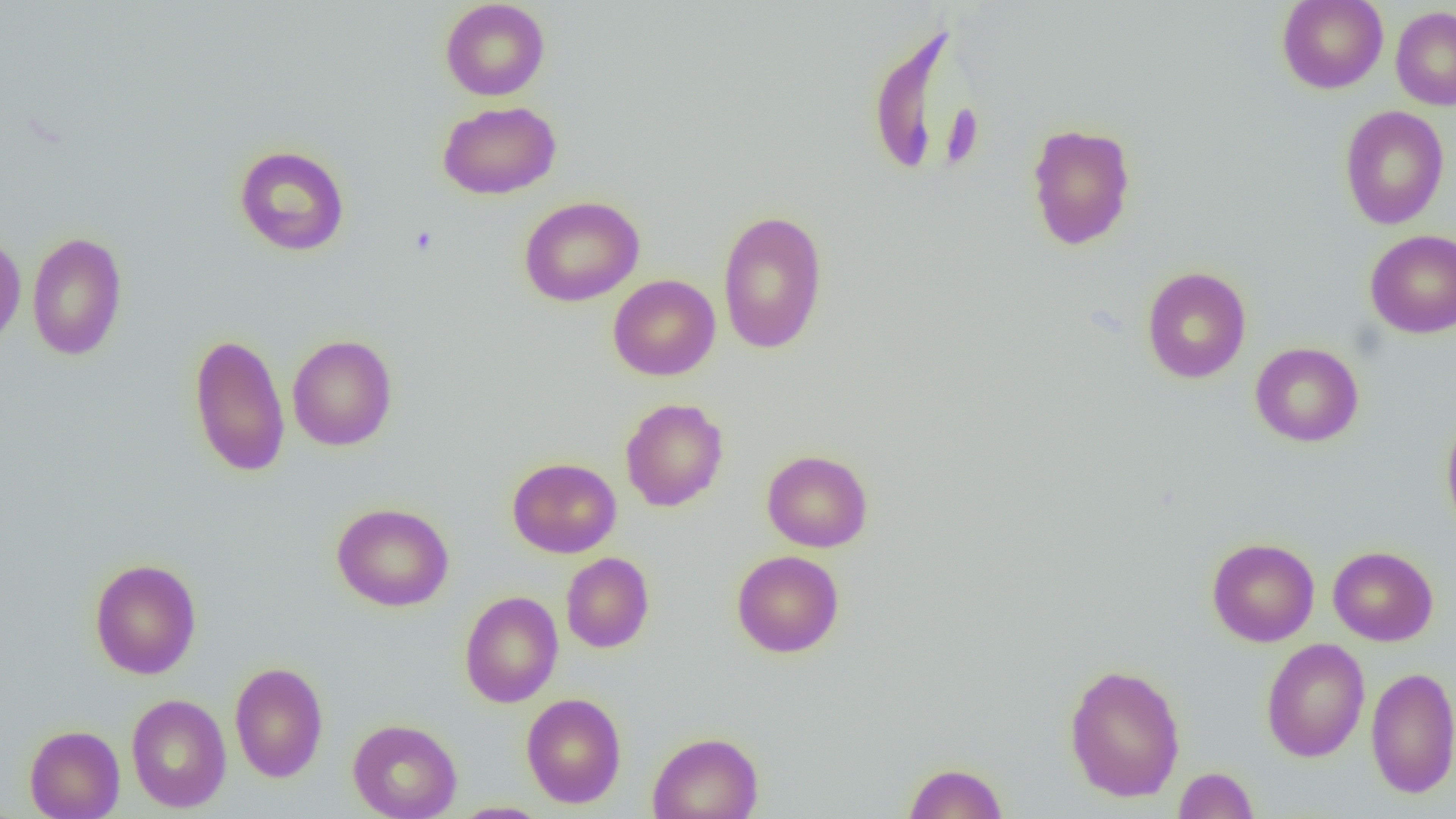

{
  "slide_level_diagnosis": "negative for blood parasites",
  "preparation": "thin blood film",
  "magnification": "1000x",
  "modality": "light microscopy",
  "uninfected_red_blood_cell_locations": "approximate bounding boxes as named x1/y1/x2/y2 corners in pixels: (x1=440, y1=0, x2=550, y2=101), (x1=1277, y1=0, x2=1388, y2=93), (x1=1390, y1=6, x2=1456, y2=110), (x1=867, y1=25, x2=971, y2=180), (x1=437, y1=101, x2=562, y2=199), (x1=1339, y1=105, x2=1450, y2=229), (x1=1026, y1=122, x2=1137, y2=251), (x1=234, y1=145, x2=350, y2=256), (x1=519, y1=195, x2=644, y2=306), (x1=717, y1=209, x2=828, y2=355), (x1=1364, y1=229, x2=1456, y2=337), (x1=27, y1=231, x2=128, y2=361), (x1=0, y1=232, x2=26, y2=350), (x1=1142, y1=266, x2=1251, y2=384), (x1=608, y1=274, x2=720, y2=380), (x1=188, y1=332, x2=291, y2=478), (x1=287, y1=334, x2=398, y2=451), (x1=1250, y1=342, x2=1363, y2=447), (x1=620, y1=398, x2=729, y2=512), (x1=1441, y1=414, x2=1456, y2=539), (x1=762, y1=450, x2=873, y2=553), (x1=507, y1=457, x2=621, y2=558), (x1=331, y1=502, x2=454, y2=612), (x1=1207, y1=537, x2=1319, y2=647), (x1=1327, y1=546, x2=1438, y2=646), (x1=731, y1=550, x2=844, y2=658), (x1=561, y1=552, x2=654, y2=653), (x1=89, y1=558, x2=202, y2=679), (x1=459, y1=590, x2=563, y2=708), (x1=1261, y1=638, x2=1370, y2=762), (x1=229, y1=661, x2=328, y2=783), (x1=1064, y1=663, x2=1185, y2=802), (x1=1366, y1=667, x2=1456, y2=798), (x1=521, y1=692, x2=627, y2=809), (x1=126, y1=694, x2=231, y2=813), (x1=348, y1=718, x2=462, y2=819), (x1=24, y1=725, x2=125, y2=818), (x1=647, y1=731, x2=764, y2=819), (x1=903, y1=762, x2=1008, y2=818), (x1=1174, y1=767, x2=1259, y2=819), (x1=449, y1=802, x2=552, y2=819)",
  "field_of_view": "single",
  "image_size": "1456×819 pixels"
}